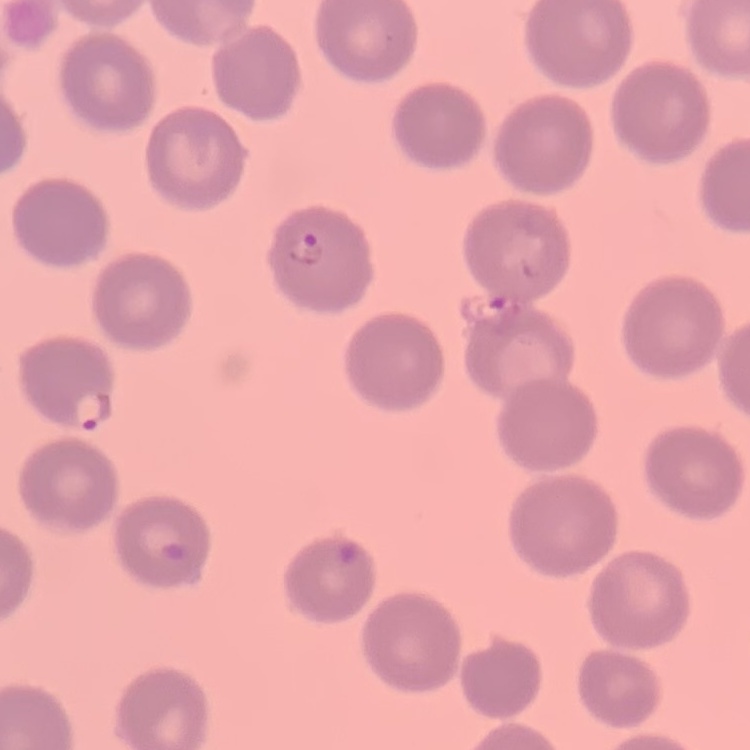

Summary:
  - Erythrocyte morphology: no rouleaux formation
  - Preparation: thin peripheral smear
  - Stain: Field's or Giemsa
  - Image type: one tile cut from a larger photomicrograph